Assess this cell for malaria.
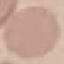
It is uninfected.

Thin blood smear. Automatically extracted cell patch, resized to 64 × 64 pixels. Acquired by smartphone through the microscope eyepiece. Giemsa stain.